Assess the morphology of the red blood cells.
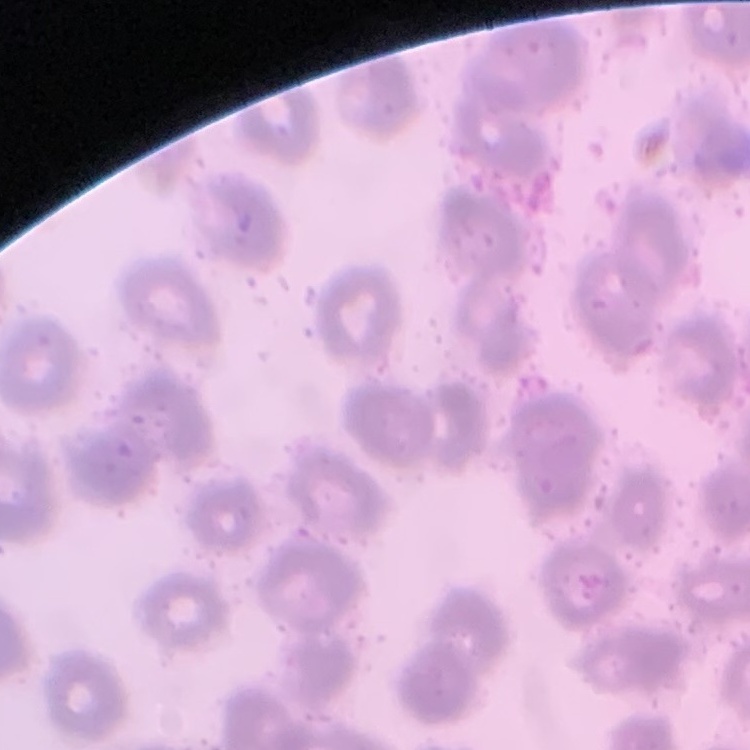
They show no rouleaux formation.

Summary:
  - Preparation: thin blood smear
  - Stain: Field's or Giemsa
  - Image type: one tile cut from a larger photomicrograph